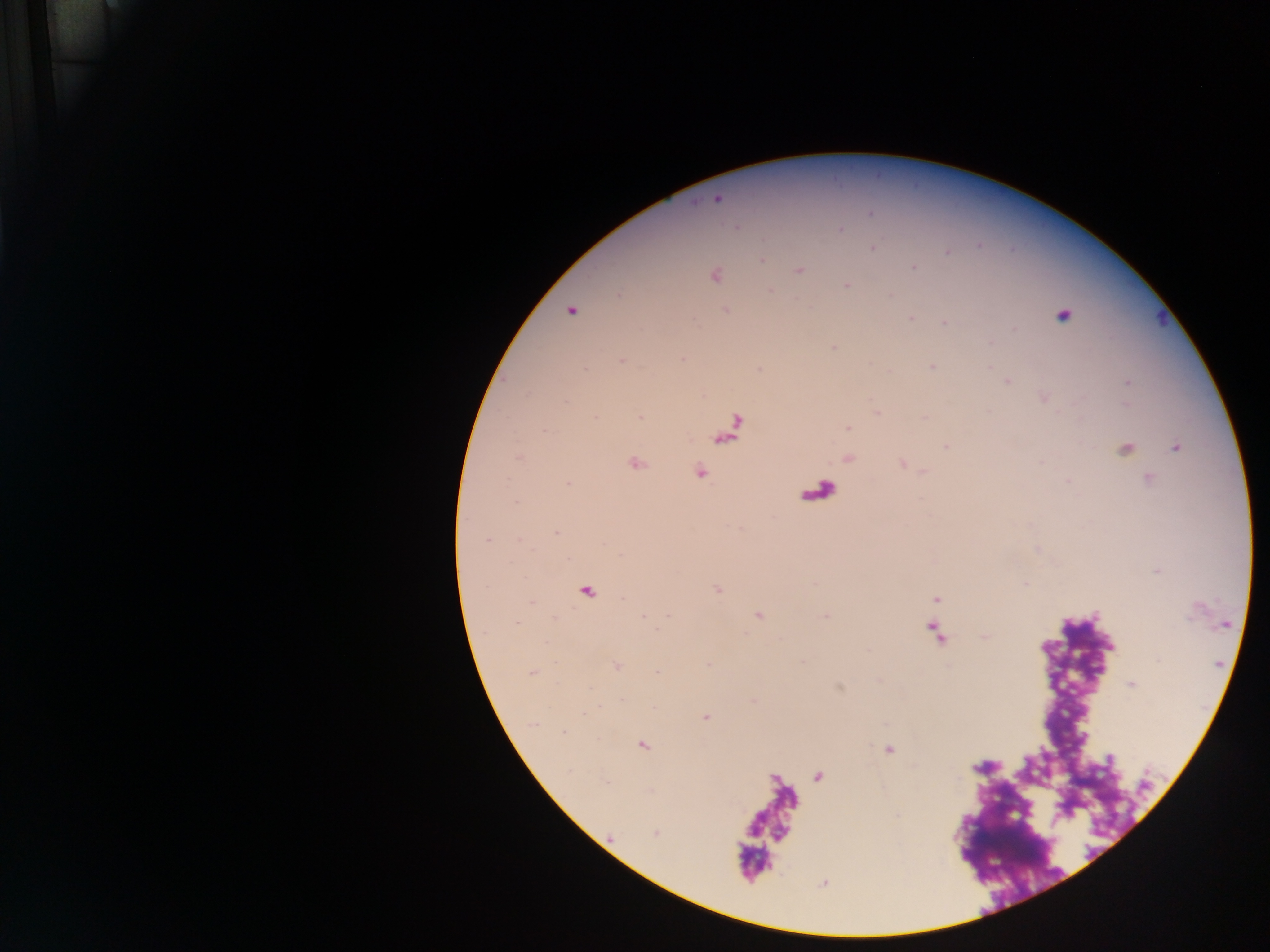 Approximate centers as [x, y] in pixels. Malaria parasite locations: [717, 199], [871, 213], [735, 227], [841, 229], [872, 248], [947, 252], [762, 260], [913, 267], [798, 271], [715, 276], [846, 285], [725, 310], [570, 311], [1063, 315], [910, 318], [944, 323], [834, 347], [682, 358], [622, 360], [931, 367], [1007, 381], [1128, 383], [1044, 397], [876, 412], [640, 417], [595, 418], [848, 428], [946, 446], [1176, 448], [1125, 449], [519, 458], [635, 463], [700, 472], [1148, 479], [1068, 481], [568, 484], [516, 501], [556, 532], [487, 540], [1026, 583], [935, 599], [531, 602], [669, 615], [757, 615], [643, 616], [985, 636], [618, 666], [532, 672], [657, 672], [1131, 683], [622, 699], [754, 701], [706, 717], [564, 731], [643, 746], [889, 749], [605, 782], [655, 833]. Leukocyte locations: [732, 428], [588, 591]. Mobile-phone photograph taken through the microscope. Collected in Ghana. Image is 1270×952 pixels. Thick blood film. One field of view.